Identify the preparation type.
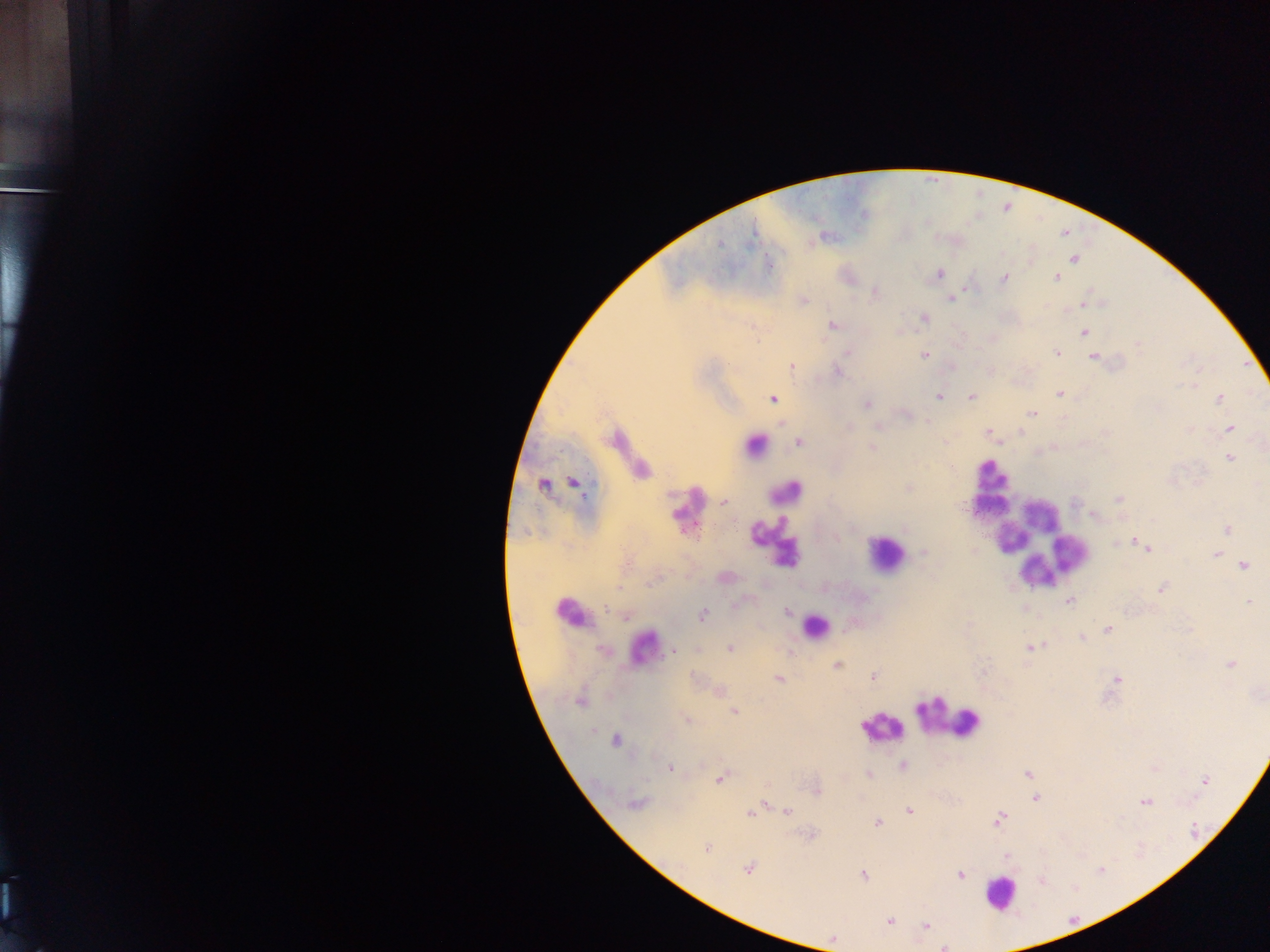

Thick blood film.

Approximate centers as [x, y] in pixels.
Summary:
  - Leukocyte locations: [751, 451], [989, 470], [793, 494], [988, 507], [1048, 512], [1011, 540], [769, 552], [1077, 553], [882, 556], [1041, 571], [568, 618], [812, 628], [646, 648], [950, 717], [883, 728], [1003, 890]
  - Malaria parasite locations: [821, 237], [1074, 260], [767, 265], [938, 274], [1004, 276], [1056, 279], [1005, 280], [950, 298], [1083, 307], [924, 319], [832, 326], [1084, 331], [1138, 344], [846, 352], [1057, 353], [925, 355], [1092, 357], [790, 366], [836, 371], [1195, 383], [1057, 393], [938, 396], [971, 397], [1220, 398], [866, 403], [1032, 415], [782, 423], [877, 426], [1229, 428], [988, 433], [799, 442], [872, 448], [1228, 456], [1119, 499], [722, 502], [1094, 514], [1133, 540], [1115, 544], [975, 548], [1148, 551], [1216, 555], [1244, 565], [1160, 589], [1069, 600], [1248, 600], [787, 612], [703, 615], [624, 617], [1107, 630], [1081, 637], [730, 647], [1028, 647], [602, 649], [673, 650], [838, 664], [1230, 664], [874, 676], [1116, 678], [779, 679], [735, 710], [687, 719], [616, 740], [903, 765], [671, 769], [869, 774], [720, 778], [1203, 782], [1036, 799], [766, 803], [1144, 803], [638, 805], [758, 808], [787, 811], [909, 811], [750, 815], [999, 819], [877, 821], [706, 849], [749, 868], [863, 875], [963, 875], [890, 922], [927, 924], [832, 940], [944, 945]
  - Field of view: single
  - Country: Ghana
  - Capture: mobile-phone photograph through a microscope
  - Image size: 1270×952 pixels